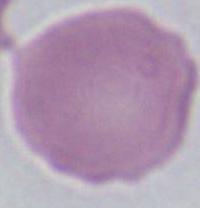
Summary:
  - Magnification: 1000x
  - Modality: micrograph
  - Identification: red blood cell